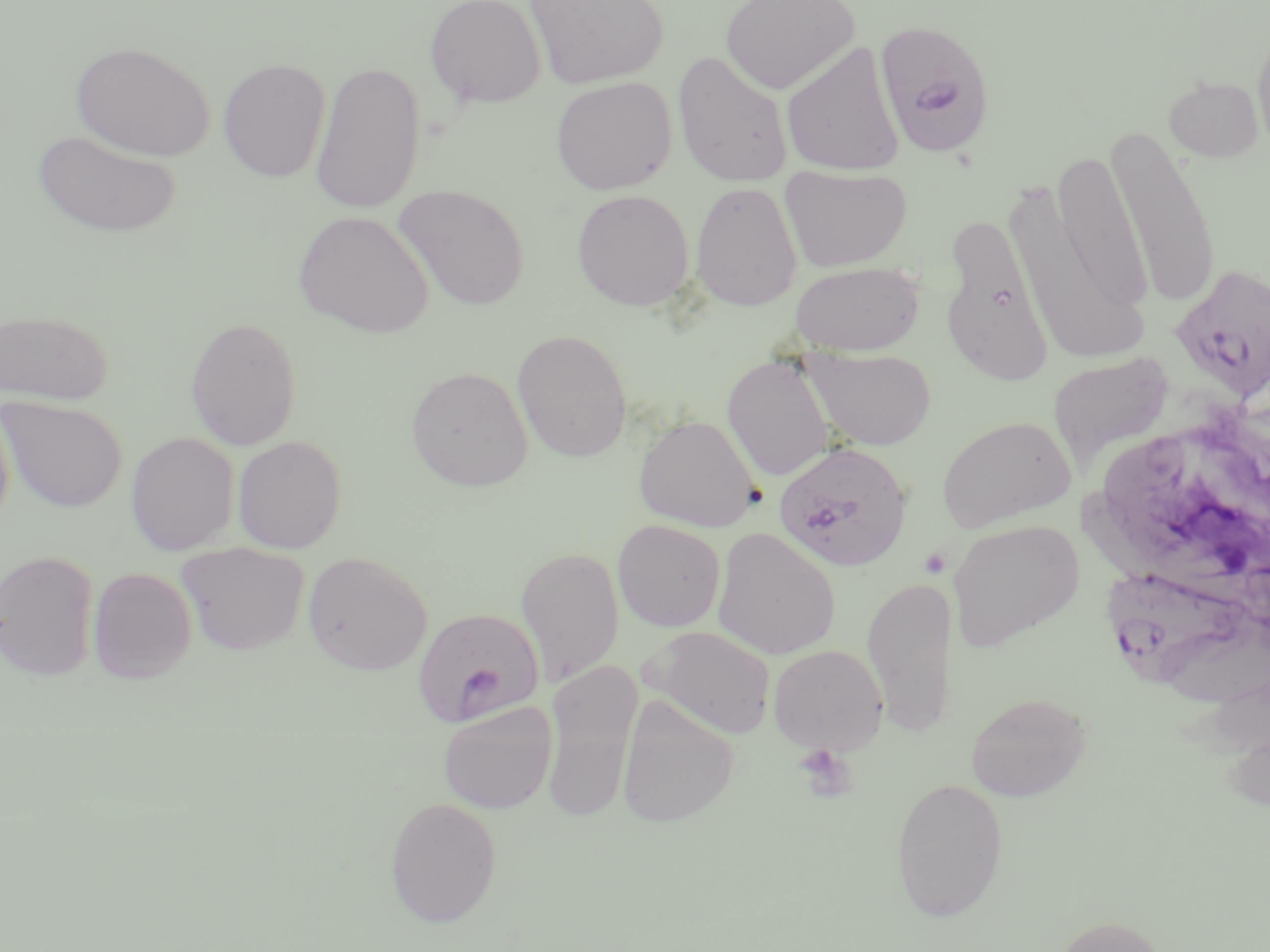

Approximate bounding boxes as named x1/y1/x2/y2 corners in pixels. Uninfected red blood cell locations: (x1=424, y1=0, x2=546, y2=108), (x1=525, y1=0, x2=669, y2=88), (x1=720, y1=0, x2=860, y2=94), (x1=1252, y1=22, x2=1270, y2=157), (x1=780, y1=40, x2=904, y2=178), (x1=71, y1=41, x2=215, y2=161), (x1=672, y1=50, x2=793, y2=188), (x1=218, y1=59, x2=331, y2=182), (x1=310, y1=60, x2=426, y2=214), (x1=1163, y1=75, x2=1264, y2=162), (x1=550, y1=76, x2=677, y2=195), (x1=1106, y1=119, x2=1222, y2=312), (x1=32, y1=129, x2=181, y2=238), (x1=1053, y1=147, x2=1152, y2=315), (x1=779, y1=165, x2=913, y2=272), (x1=689, y1=181, x2=803, y2=312), (x1=394, y1=184, x2=530, y2=311), (x1=1011, y1=184, x2=1153, y2=362), (x1=571, y1=189, x2=694, y2=311), (x1=294, y1=211, x2=433, y2=338), (x1=940, y1=215, x2=1054, y2=384), (x1=790, y1=261, x2=924, y2=355), (x1=1, y1=309, x2=114, y2=405), (x1=184, y1=316, x2=302, y2=450), (x1=512, y1=329, x2=632, y2=463), (x1=802, y1=348, x2=936, y2=451), (x1=1047, y1=352, x2=1175, y2=466), (x1=722, y1=355, x2=834, y2=481), (x1=406, y1=366, x2=534, y2=491), (x1=0, y1=397, x2=127, y2=512), (x1=0, y1=402, x2=14, y2=533), (x1=633, y1=414, x2=762, y2=533), (x1=936, y1=415, x2=1077, y2=532), (x1=126, y1=432, x2=239, y2=556), (x1=232, y1=435, x2=347, y2=554), (x1=1080, y1=488, x2=1270, y2=617), (x1=612, y1=519, x2=726, y2=632), (x1=946, y1=519, x2=1084, y2=652), (x1=711, y1=528, x2=841, y2=660), (x1=176, y1=542, x2=310, y2=656), (x1=515, y1=546, x2=624, y2=688), (x1=0, y1=548, x2=99, y2=681), (x1=302, y1=551, x2=433, y2=676), (x1=87, y1=567, x2=197, y2=684), (x1=862, y1=575, x2=956, y2=737), (x1=644, y1=625, x2=777, y2=739), (x1=768, y1=645, x2=888, y2=754), (x1=540, y1=658, x2=643, y2=823), (x1=966, y1=691, x2=1092, y2=802), (x1=616, y1=695, x2=739, y2=828), (x1=437, y1=701, x2=557, y2=814), (x1=890, y1=776, x2=1009, y2=923), (x1=384, y1=796, x2=503, y2=927), (x1=1051, y1=914, x2=1170, y2=952). Platelet locations: (x1=918, y1=546, x2=951, y2=579), (x1=793, y1=743, x2=857, y2=802). Plasmodium falciparum-infected red blood cell locations: (x1=874, y1=19, x2=996, y2=158), (x1=1169, y1=264, x2=1270, y2=403), (x1=774, y1=440, x2=912, y2=572), (x1=1107, y1=573, x2=1270, y2=702), (x1=411, y1=608, x2=552, y2=729). Slide-level diagnosis: Plasmodium falciparum. 1000x magnification. May-Grünwald-Giemsa stain. Thin blood film. Single field of view. Image is 1270×952 pixels. Light microscopy.